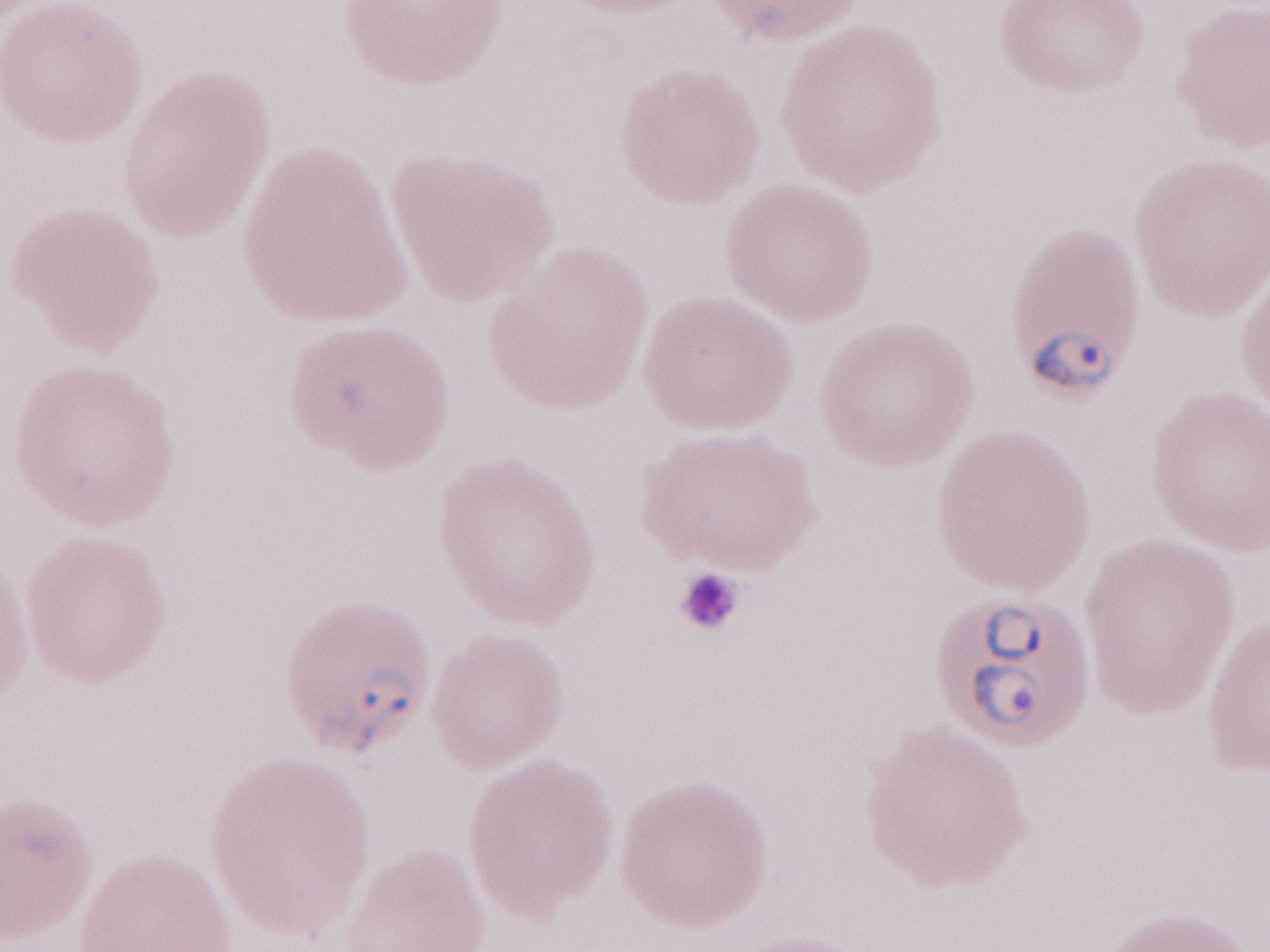 Magnification: 1,000x. May-Grünwald-Giemsa stain. Thin blood smear. Image is 1270×952 pixels. Malaria diagnosis (patient-level): positive. Olympus BX43 microscope, Olympus DP73 camera. Single field of view.